State which parasite is depicted.
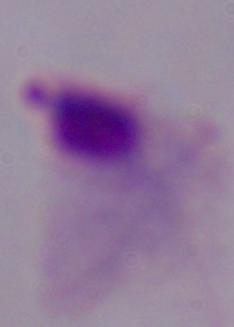

A trichomonad.

magnification = 1000x
modality = micrograph